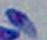
Summary:
  - Modality: photomicrograph
  - Identification: Toxoplasma gondii
  - Magnification: 1000x